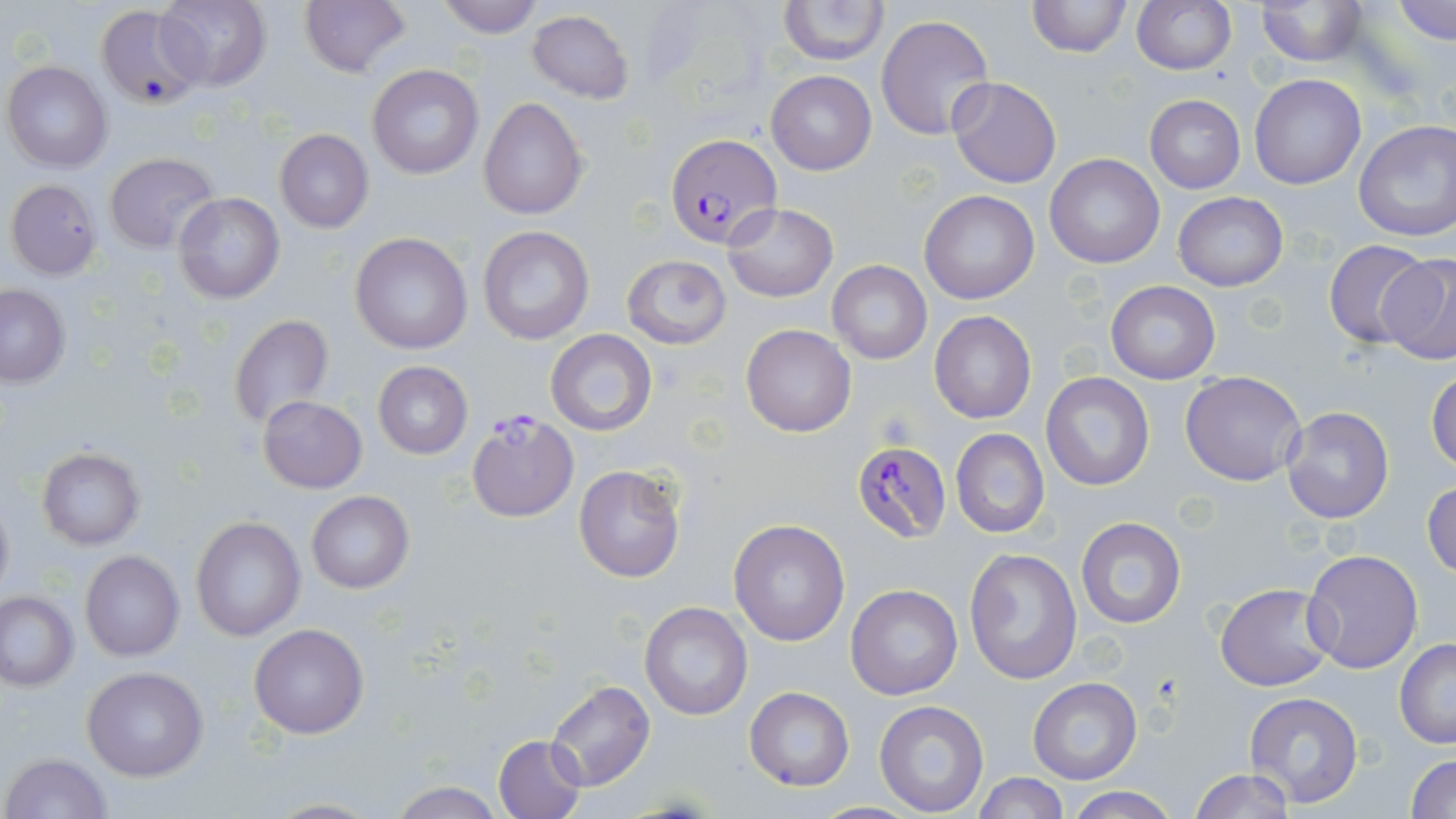 Approximate bounding boxes as (x1,y1)-(x2,y2) corner pairs in pixels. Plasmodium falciparum-infected red blood cell locations: (663,133)-(782,246), (465,409)-(577,520), (850,440)-(954,545). Uninfected red blood cell locations: (154,0)-(272,92), (299,0)-(409,77), (435,0)-(544,37), (1025,0)-(1130,57), (1131,0)-(1237,75), (1252,0)-(1369,67), (1392,0)-(1456,45), (777,2)-(890,66), (95,4)-(206,111), (527,11)-(634,104), (876,14)-(994,140), (3,60)-(112,172), (368,65)-(484,180), (767,71)-(876,174), (1248,74)-(1366,190), (947,76)-(1061,188), (1144,94)-(1245,193), (480,97)-(588,220), (1352,122)-(1456,243), (274,129)-(373,233), (103,151)-(218,253), (1044,153)-(1165,269), (5,179)-(102,279), (919,190)-(1039,304), (1173,192)-(1288,291), (173,193)-(284,303), (723,202)-(838,301), (477,226)-(596,345), (349,233)-(472,354), (1323,239)-(1434,350), (1377,251)-(1456,363), (621,254)-(731,347), (827,260)-(932,365), (1104,280)-(1220,384), (0,284)-(70,386), (929,310)-(1036,424), (227,314)-(335,432), (740,323)-(856,437), (546,330)-(658,437), (372,361)-(473,457), (1426,366)-(1456,473), (1180,370)-(1307,486), (1040,373)-(1154,491), (258,396)-(367,493), (1281,405)-(1395,525), (950,428)-(1049,538), (36,446)-(145,548), (573,463)-(686,584), (1422,479)-(1455,580), (305,491)-(412,593), (0,494)-(14,602), (191,516)-(306,640), (1075,516)-(1186,629), (729,519)-(851,648), (963,546)-(1083,687), (1303,548)-(1424,674), (80,550)-(184,661), (1216,582)-(1335,692), (845,584)-(962,701), (1,591)-(78,691), (639,601)-(752,721), (249,622)-(369,739), (1393,639)-(1456,748), (83,666)-(208,781), (1028,677)-(1143,784), (543,680)-(657,791), (743,687)-(854,791), (1243,693)-(1365,810), (875,700)-(989,816), (493,734)-(585,819), (2,752)-(112,819), (1407,753)-(1456,819), (1187,769)-(1298,818), (973,773)-(1069,818), (387,782)-(506,818), (1062,786)-(1179,819), (256,798)-(386,818). Slide-level diagnosis: Plasmodium falciparum. May-Grünwald-Giemsa stain. Single field of view. Thin blood smear. Image is 1456×819 pixels. 1000x magnification. Optical microscopy.